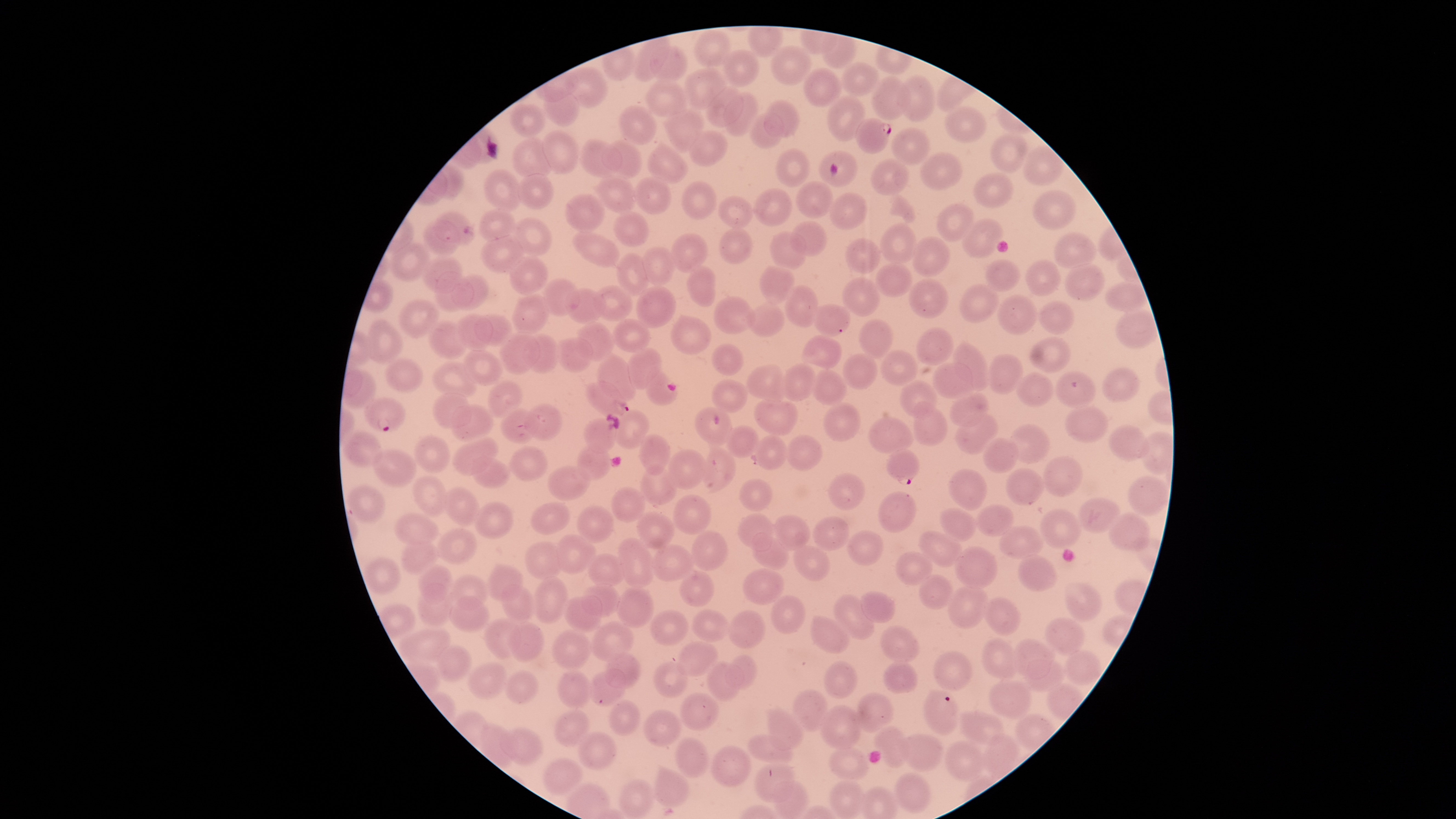

{
  "parasitized_red_blood_cells": "approximate bounding boxes, in pixels from the top-left corner: (left=855, top=118, right=892, bottom=154), (left=584, top=380, right=629, bottom=417), (left=364, top=396, right=406, bottom=432), (left=886, top=449, right=921, bottom=486)",
  "visible_region": "circular",
  "species": "Plasmodium falciparum",
  "field_of_view": "single",
  "capture": "smartphone photograph through the microscope eyepiece",
  "uninfected_red_blood_cells": "approximate bounding boxes, in pixels from the top-left corner: (left=695, top=30, right=731, bottom=68), (left=634, top=38, right=669, bottom=82), (left=771, top=45, right=811, bottom=86), (left=650, top=46, right=687, bottom=83), (left=722, top=49, right=758, bottom=88), (left=842, top=62, right=879, bottom=96), (left=568, top=66, right=608, bottom=108), (left=804, top=67, right=840, bottom=108), (left=684, top=68, right=726, bottom=110), (left=898, top=74, right=935, bottom=123), (left=871, top=75, right=910, bottom=119), (left=646, top=79, right=686, bottom=117), (left=543, top=88, right=580, bottom=127), (left=705, top=88, right=743, bottom=128), (left=724, top=93, right=759, bottom=136), (left=827, top=94, right=865, bottom=142), (left=764, top=100, right=799, bottom=138), (left=510, top=103, right=545, bottom=137), (left=619, top=105, right=656, bottom=144), (left=946, top=106, right=987, bottom=145), (left=667, top=109, right=703, bottom=151), (left=748, top=114, right=784, bottom=149), (left=892, top=127, right=930, bottom=166), (left=542, top=130, right=579, bottom=174), (left=688, top=131, right=727, bottom=166), (left=992, top=133, right=1027, bottom=174), (left=512, top=139, right=554, bottom=178), (left=580, top=139, right=623, bottom=177), (left=602, top=141, right=643, bottom=178), (left=648, top=145, right=688, bottom=183), (left=1021, top=147, right=1063, bottom=185), (left=775, top=148, right=811, bottom=188), (left=818, top=150, right=856, bottom=188), (left=922, top=152, right=962, bottom=191), (left=871, top=159, right=910, bottom=197), (left=482, top=168, right=522, bottom=211), (left=596, top=172, right=638, bottom=214), (left=972, top=173, right=1014, bottom=208), (left=517, top=174, right=555, bottom=210), (left=633, top=177, right=671, bottom=214), (left=681, top=181, right=716, bottom=220), (left=795, top=181, right=833, bottom=218), (left=754, top=188, right=793, bottom=226), (left=1032, top=189, right=1078, bottom=229), (left=564, top=193, right=606, bottom=233), (left=830, top=193, right=867, bottom=230), (left=718, top=196, right=753, bottom=229), (left=935, top=203, right=975, bottom=242), (left=479, top=209, right=515, bottom=243), (left=435, top=210, right=474, bottom=244), (left=613, top=211, right=649, bottom=247), (left=515, top=217, right=552, bottom=257), (left=422, top=219, right=461, bottom=255), (left=960, top=219, right=1004, bottom=258), (left=791, top=222, right=826, bottom=256), (left=879, top=224, right=918, bottom=263), (left=719, top=228, right=752, bottom=264), (left=574, top=231, right=618, bottom=268), (left=771, top=231, right=806, bottom=271), (left=1052, top=232, right=1098, bottom=270), (left=482, top=234, right=523, bottom=274), (left=670, top=234, right=708, bottom=273), (left=912, top=236, right=950, bottom=277), (left=844, top=238, right=881, bottom=274), (left=390, top=242, right=431, bottom=280), (left=642, top=246, right=675, bottom=286), (left=617, top=253, right=651, bottom=295), (left=423, top=256, right=462, bottom=293), (left=510, top=256, right=547, bottom=294), (left=983, top=259, right=1021, bottom=292), (left=1025, top=260, right=1060, bottom=295), (left=1064, top=262, right=1104, bottom=301), (left=875, top=263, right=913, bottom=297), (left=687, top=265, right=715, bottom=307), (left=759, top=267, right=795, bottom=304), (left=434, top=272, right=473, bottom=312), (left=452, top=273, right=488, bottom=311), (left=543, top=278, right=580, bottom=316), (left=842, top=278, right=881, bottom=316), (left=908, top=278, right=947, bottom=318), (left=1104, top=282, right=1147, bottom=312), (left=959, top=284, right=999, bottom=323), (left=593, top=285, right=631, bottom=321), (left=785, top=285, right=819, bottom=327), (left=636, top=286, right=676, bottom=329), (left=566, top=288, right=605, bottom=324), (left=511, top=293, right=548, bottom=336), (left=997, top=295, right=1038, bottom=335), (left=713, top=297, right=753, bottom=335), (left=400, top=298, right=438, bottom=338), (left=1038, top=301, right=1075, bottom=335), (left=748, top=302, right=784, bottom=337), (left=813, top=305, right=851, bottom=335), (left=1115, top=311, right=1156, bottom=349), (left=456, top=312, right=493, bottom=350), (left=474, top=314, right=514, bottom=344), (left=670, top=315, right=710, bottom=355), (left=368, top=319, right=403, bottom=363), (left=612, top=319, right=650, bottom=353), (left=858, top=319, right=893, bottom=359), (left=428, top=320, right=467, bottom=359), (left=576, top=323, right=615, bottom=362), (left=916, top=327, right=953, bottom=367), (left=499, top=332, right=539, bottom=375), (left=524, top=334, right=559, bottom=374), (left=801, top=334, right=842, bottom=370), (left=555, top=337, right=593, bottom=372), (left=1028, top=337, right=1072, bottom=373), (left=952, top=341, right=990, bottom=389), (left=711, top=343, right=744, bottom=376), (left=464, top=348, right=502, bottom=385), (left=627, top=348, right=662, bottom=389), (left=881, top=349, right=917, bottom=386), (left=842, top=353, right=877, bottom=390), (left=989, top=353, right=1024, bottom=393), (left=597, top=354, right=636, bottom=402), (left=387, top=357, right=423, bottom=393), (left=430, top=361, right=476, bottom=397), (left=933, top=362, right=973, bottom=399), (left=781, top=363, right=816, bottom=401), (left=747, top=365, right=785, bottom=401), (left=1102, top=367, right=1139, bottom=402), (left=811, top=369, right=846, bottom=406), (left=646, top=370, right=678, bottom=406), (left=1055, top=371, right=1095, bottom=408), (left=1015, top=373, right=1053, bottom=407), (left=712, top=379, right=748, bottom=413), (left=487, top=380, right=523, bottom=418), (left=899, top=380, right=938, bottom=419), (left=433, top=392, right=470, bottom=429), (left=950, top=392, right=988, bottom=426), (left=753, top=398, right=798, bottom=436), (left=913, top=402, right=947, bottom=446), (left=452, top=404, right=491, bottom=442), (left=524, top=405, right=562, bottom=440), (left=822, top=405, right=860, bottom=442), (left=500, top=407, right=537, bottom=444), (left=694, top=407, right=732, bottom=446), (left=1065, top=407, right=1108, bottom=443), (left=612, top=409, right=649, bottom=449), (left=955, top=414, right=999, bottom=454), (left=867, top=416, right=914, bottom=454), (left=584, top=418, right=618, bottom=454), (left=1010, top=423, right=1048, bottom=464), (left=725, top=425, right=760, bottom=457), (left=1109, top=425, right=1149, bottom=463), (left=343, top=431, right=383, bottom=467), (left=414, top=435, right=449, bottom=473), (left=639, top=435, right=671, bottom=475), (left=754, top=436, right=788, bottom=469), (left=785, top=436, right=822, bottom=471), (left=452, top=437, right=498, bottom=476), (left=983, top=438, right=1018, bottom=473), (left=576, top=444, right=611, bottom=480), (left=510, top=446, right=546, bottom=482), (left=702, top=447, right=734, bottom=491), (left=667, top=449, right=708, bottom=488), (left=371, top=450, right=417, bottom=487), (left=1043, top=455, right=1082, bottom=498), (left=471, top=457, right=510, bottom=488), (left=640, top=464, right=678, bottom=505), (left=546, top=465, right=590, bottom=500), (left=1006, top=467, right=1043, bottom=506), (left=948, top=469, right=987, bottom=511), (left=828, top=472, right=864, bottom=511), (left=414, top=475, right=446, bottom=517), (left=1128, top=475, right=1169, bottom=517), (left=739, top=478, right=772, bottom=511), (left=347, top=484, right=385, bottom=524), (left=443, top=486, right=480, bottom=527), (left=611, top=487, right=645, bottom=522), (left=878, top=490, right=916, bottom=533), (left=672, top=494, right=712, bottom=534), (left=1078, top=496, right=1121, bottom=534), (left=474, top=502, right=513, bottom=539), (left=530, top=503, right=569, bottom=535), (left=976, top=504, right=1014, bottom=536), (left=577, top=505, right=613, bottom=542), (left=939, top=507, right=975, bottom=540), (left=1040, top=507, right=1083, bottom=550), (left=1108, top=511, right=1150, bottom=552), (left=393, top=512, right=440, bottom=546), (left=637, top=512, right=675, bottom=549), (left=738, top=514, right=773, bottom=551), (left=772, top=514, right=810, bottom=551), (left=813, top=516, right=850, bottom=551), (left=1000, top=526, right=1043, bottom=558), (left=437, top=528, right=476, bottom=563), (left=847, top=529, right=883, bottom=566), (left=919, top=530, right=963, bottom=568), (left=692, top=531, right=727, bottom=571), (left=751, top=533, right=789, bottom=570), (left=556, top=535, right=595, bottom=572), (left=399, top=538, right=436, bottom=574), (left=617, top=539, right=654, bottom=587), (left=524, top=542, right=562, bottom=581), (left=792, top=544, right=830, bottom=581), (left=954, top=545, right=997, bottom=590), (left=650, top=546, right=695, bottom=582), (left=895, top=550, right=932, bottom=586), (left=587, top=552, right=626, bottom=588), (left=1018, top=554, right=1057, bottom=591), (left=363, top=559, right=400, bottom=593), (left=418, top=563, right=452, bottom=604), (left=487, top=564, right=524, bottom=602), (left=742, top=568, right=783, bottom=604), (left=679, top=572, right=714, bottom=607), (left=450, top=574, right=488, bottom=610), (left=918, top=575, right=953, bottom=611), (left=532, top=577, right=567, bottom=623), (left=1065, top=581, right=1103, bottom=622), (left=500, top=583, right=537, bottom=624), (left=582, top=585, right=620, bottom=616), (left=947, top=585, right=988, bottom=629), (left=616, top=587, right=655, bottom=627), (left=415, top=591, right=450, bottom=627), (left=861, top=591, right=895, bottom=622), (left=832, top=594, right=873, bottom=640), (left=562, top=595, right=601, bottom=632), (left=771, top=595, right=804, bottom=635), (left=449, top=596, right=489, bottom=632), (left=983, top=597, right=1022, bottom=636), (left=691, top=609, right=730, bottom=642), (left=650, top=610, right=689, bottom=646), (left=728, top=610, right=765, bottom=649), (left=810, top=615, right=850, bottom=653), (left=1045, top=617, right=1085, bottom=655), (left=483, top=619, right=521, bottom=657), (left=592, top=621, right=633, bottom=661), (left=507, top=623, right=543, bottom=661), (left=880, top=625, right=921, bottom=664), (left=401, top=628, right=450, bottom=665), (left=551, top=629, right=592, bottom=670), (left=981, top=638, right=1019, bottom=678), (left=1014, top=639, right=1052, bottom=679), (left=676, top=641, right=718, bottom=677), (left=436, top=644, right=471, bottom=681), (left=933, top=649, right=972, bottom=692), (left=1063, top=651, right=1100, bottom=685), (left=605, top=652, right=641, bottom=689), (left=725, top=655, right=757, bottom=690), (left=1025, top=660, right=1065, bottom=692), (left=653, top=661, right=686, bottom=699), (left=707, top=661, right=743, bottom=701), (left=822, top=661, right=858, bottom=698), (left=882, top=661, right=917, bottom=693), (left=467, top=662, right=506, bottom=699), (left=589, top=669, right=627, bottom=706), (left=504, top=670, right=538, bottom=704), (left=557, top=670, right=592, bottom=708), (left=988, top=679, right=1031, bottom=719), (left=793, top=687, right=829, bottom=730), (left=923, top=689, right=959, bottom=735), (left=680, top=691, right=718, bottom=732), (left=855, top=691, right=892, bottom=731), (left=610, top=700, right=641, bottom=736), (left=820, top=704, right=861, bottom=749), (left=767, top=707, right=803, bottom=750), (left=554, top=709, right=589, bottom=746), (left=642, top=710, right=680, bottom=747), (left=959, top=710, right=1003, bottom=745), (left=875, top=726, right=909, bottom=767), (left=500, top=727, right=542, bottom=765), (left=578, top=732, right=616, bottom=770), (left=746, top=734, right=792, bottom=763), (left=901, top=734, right=942, bottom=770), (left=674, top=736, right=708, bottom=778), (left=945, top=740, right=983, bottom=781), (left=711, top=745, right=751, bottom=787), (left=828, top=749, right=868, bottom=781), (left=542, top=758, right=583, bottom=797), (left=754, top=762, right=795, bottom=804), (left=654, top=768, right=688, bottom=807), (left=894, top=773, right=930, bottom=814), (left=620, top=779, right=654, bottom=818), (left=772, top=780, right=808, bottom=818), (left=830, top=781, right=864, bottom=818)",
  "presence": "malaria parasites seen",
  "image_size": "1456×819 pixels",
  "preparation": "thin blood smear",
  "stain": "Giemsa"
}